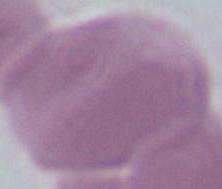 Micrograph. Captured at 1000x magnification. A red blood cell is seen.